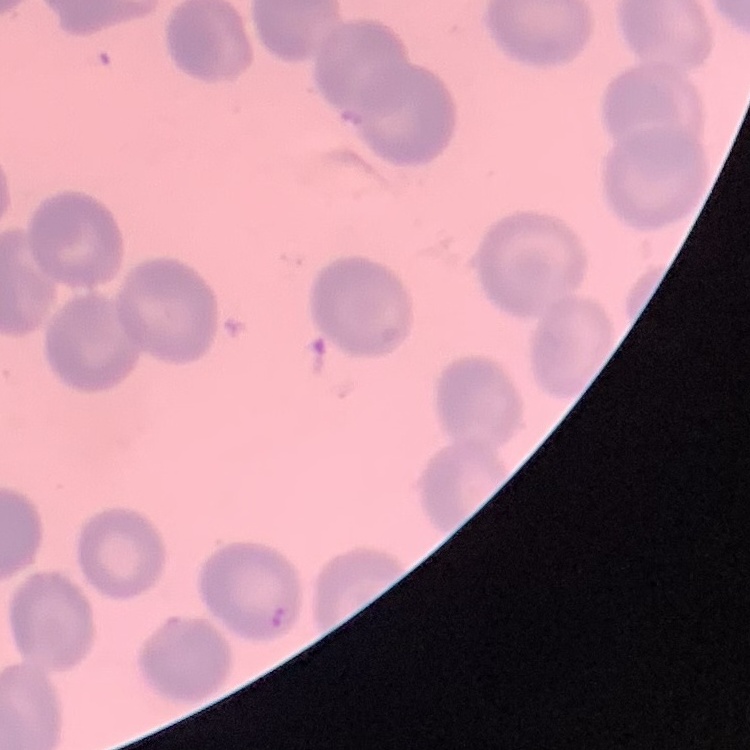 The red blood cells exhibit no rouleaux formation. Stained with either Field's or Giemsa. Thin blood smear. One tile cut from a larger photomicrograph.